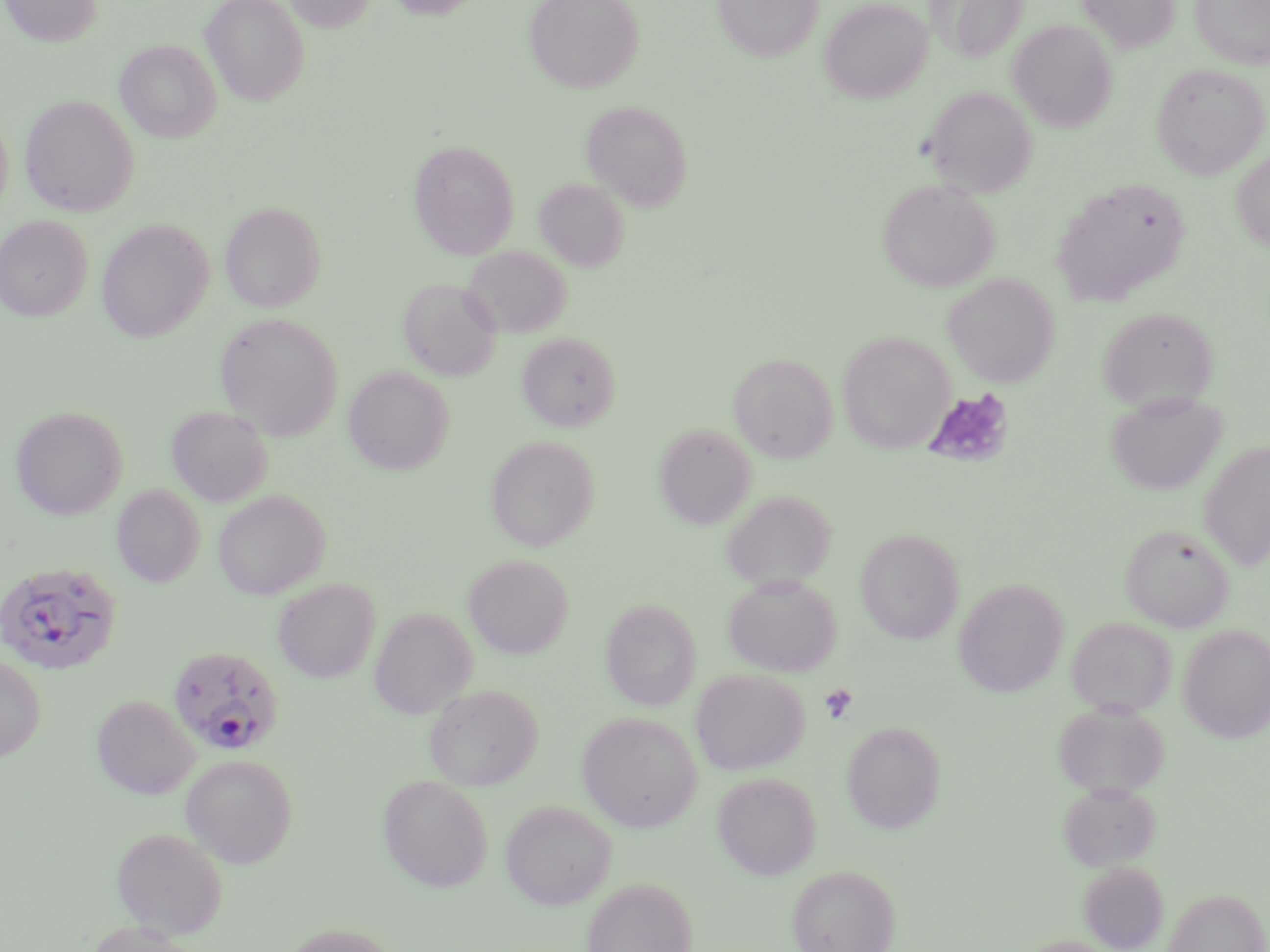
slide-level diagnosis = Plasmodium falciparum
image size = 1270×952 pixels
uninfected red blood cell locations = approximate bounding boxes as named x1/y1/x2/y2 corners in pixels: (x1=1, y1=0, x2=103, y2=46), (x1=200, y1=0, x2=310, y2=106), (x1=283, y1=0, x2=377, y2=32), (x1=386, y1=0, x2=487, y2=19), (x1=524, y1=0, x2=644, y2=93), (x1=713, y1=0, x2=824, y2=61), (x1=819, y1=0, x2=932, y2=104), (x1=928, y1=0, x2=1029, y2=63), (x1=1077, y1=0, x2=1180, y2=53), (x1=1190, y1=0, x2=1270, y2=69), (x1=1008, y1=20, x2=1117, y2=131), (x1=115, y1=39, x2=222, y2=142), (x1=1150, y1=62, x2=1269, y2=180), (x1=924, y1=85, x2=1037, y2=197), (x1=20, y1=94, x2=139, y2=217), (x1=582, y1=99, x2=693, y2=211), (x1=0, y1=111, x2=14, y2=218), (x1=409, y1=140, x2=520, y2=259), (x1=1231, y1=149, x2=1270, y2=253), (x1=1052, y1=177, x2=1191, y2=307), (x1=534, y1=179, x2=629, y2=271), (x1=877, y1=180, x2=999, y2=292), (x1=220, y1=201, x2=326, y2=312), (x1=0, y1=215, x2=92, y2=321), (x1=96, y1=219, x2=213, y2=342), (x1=463, y1=245, x2=571, y2=339), (x1=942, y1=273, x2=1059, y2=388), (x1=399, y1=277, x2=502, y2=381), (x1=1097, y1=306, x2=1219, y2=410), (x1=215, y1=312, x2=343, y2=440), (x1=837, y1=331, x2=954, y2=454), (x1=517, y1=332, x2=620, y2=431), (x1=728, y1=353, x2=838, y2=463), (x1=343, y1=365, x2=454, y2=475), (x1=1104, y1=390, x2=1228, y2=496), (x1=11, y1=405, x2=128, y2=520), (x1=166, y1=405, x2=273, y2=506), (x1=654, y1=423, x2=757, y2=530), (x1=485, y1=435, x2=599, y2=551), (x1=1198, y1=440, x2=1270, y2=571), (x1=112, y1=484, x2=205, y2=587), (x1=213, y1=489, x2=330, y2=600), (x1=721, y1=490, x2=836, y2=592), (x1=1120, y1=523, x2=1235, y2=631), (x1=856, y1=528, x2=965, y2=644), (x1=464, y1=554, x2=573, y2=658), (x1=722, y1=573, x2=841, y2=677), (x1=273, y1=579, x2=380, y2=683), (x1=954, y1=579, x2=1069, y2=697), (x1=600, y1=598, x2=701, y2=711), (x1=370, y1=607, x2=477, y2=719), (x1=1066, y1=616, x2=1177, y2=718), (x1=1178, y1=625, x2=1270, y2=743), (x1=0, y1=652, x2=46, y2=763), (x1=690, y1=668, x2=809, y2=774), (x1=424, y1=684, x2=543, y2=791), (x1=92, y1=695, x2=200, y2=799), (x1=1053, y1=702, x2=1169, y2=799), (x1=576, y1=712, x2=702, y2=832), (x1=841, y1=720, x2=946, y2=834), (x1=181, y1=754, x2=298, y2=868), (x1=712, y1=771, x2=822, y2=880), (x1=378, y1=774, x2=494, y2=892), (x1=1058, y1=782, x2=1161, y2=871), (x1=500, y1=799, x2=616, y2=909), (x1=111, y1=827, x2=228, y2=938), (x1=1078, y1=861, x2=1169, y2=951), (x1=786, y1=863, x2=901, y2=952), (x1=580, y1=877, x2=698, y2=952), (x1=1162, y1=886, x2=1269, y2=952), (x1=82, y1=920, x2=205, y2=952), (x1=279, y1=922, x2=402, y2=952), (x1=1012, y1=935, x2=1122, y2=952)
Plasmodium falciparum-infected red blood cell locations = approximate bounding boxes as named x1/y1/x2/y2 corners in pixels: (x1=0, y1=562, x2=122, y2=675), (x1=166, y1=644, x2=285, y2=756)
field of view = one of a larger specimen
stain = May-Grünwald-Giemsa
preparation = thin blood film
modality = light microscopy
platelet locations = approximate bounding boxes as named x1/y1/x2/y2 corners in pixels: (x1=922, y1=387, x2=1015, y2=469), (x1=820, y1=683, x2=859, y2=725)
magnification = 1000x